Report the malaria status of this cell.
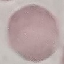

It is uninfected.

Photographed with a smartphone camera at the microscope eyepiece. Thin blood film. Cell patch, automatically extracted from a larger field of view and resized to 64 × 64 pixels. Giemsa-stained preparation.